Report the malaria status.
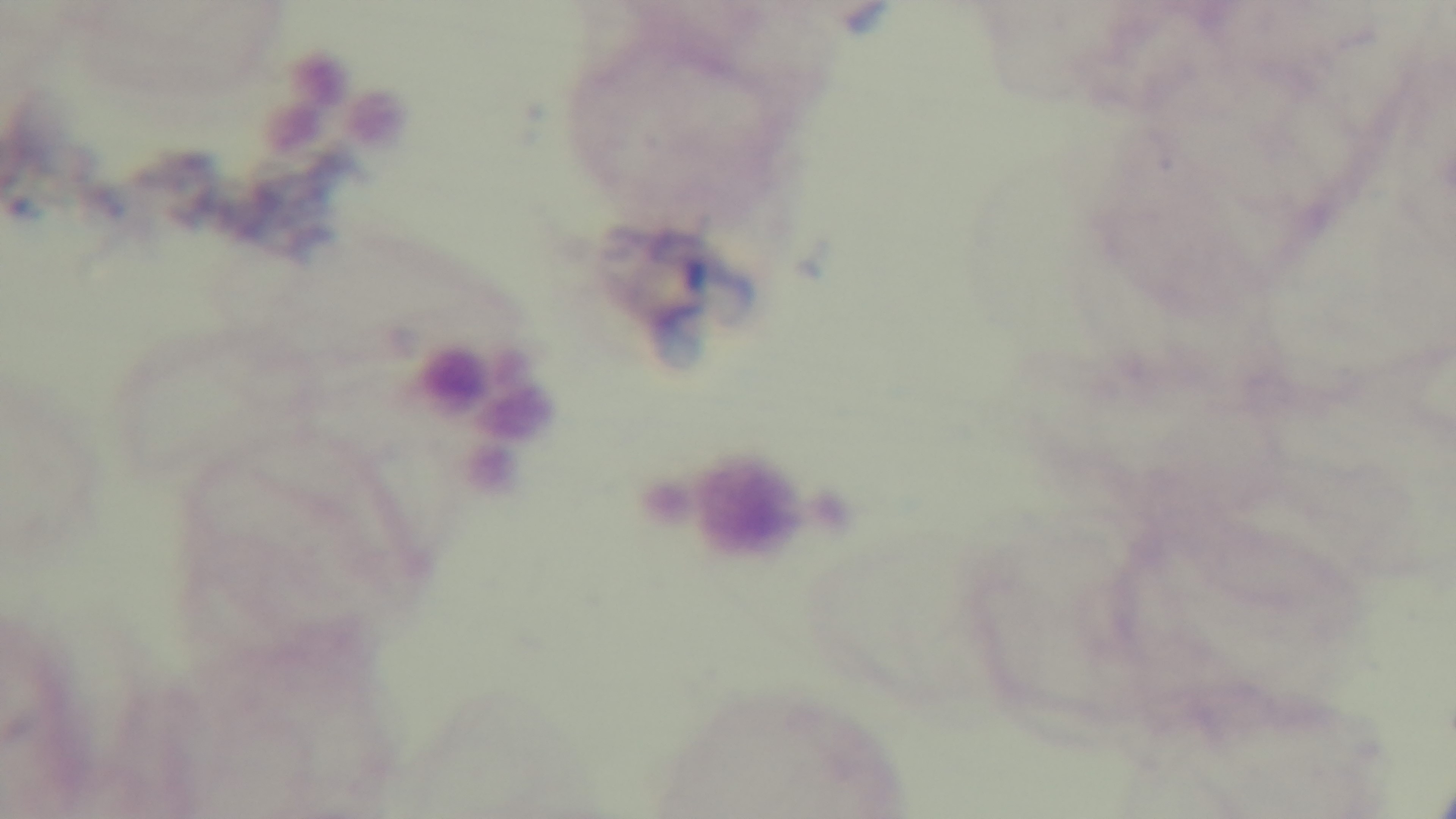

It is uninfected.

Summary:
  - Modality: light microscopy
  - Field of view: single
  - Stain: Giemsa
  - Objective: 100x oil immersion
  - Preparation: thick smear
  - Capture: mounted 4K digital camera